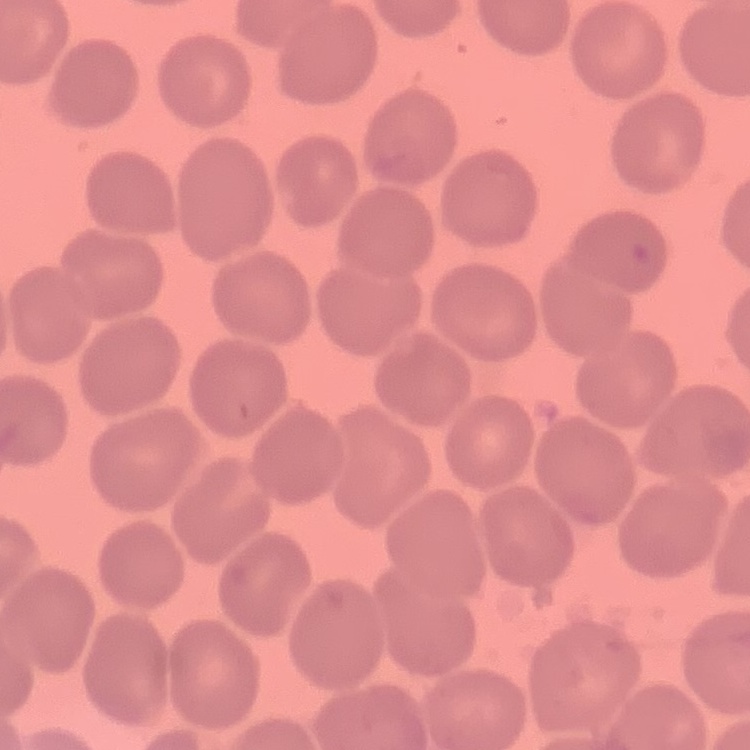
erythrocyte morphology = no rouleaux formation
preparation = thin peripheral smear
stain = Field's or Giemsa
image type = square crop of a larger photomicrograph